Outline each Plasmodium vivax-infected red blood cell.
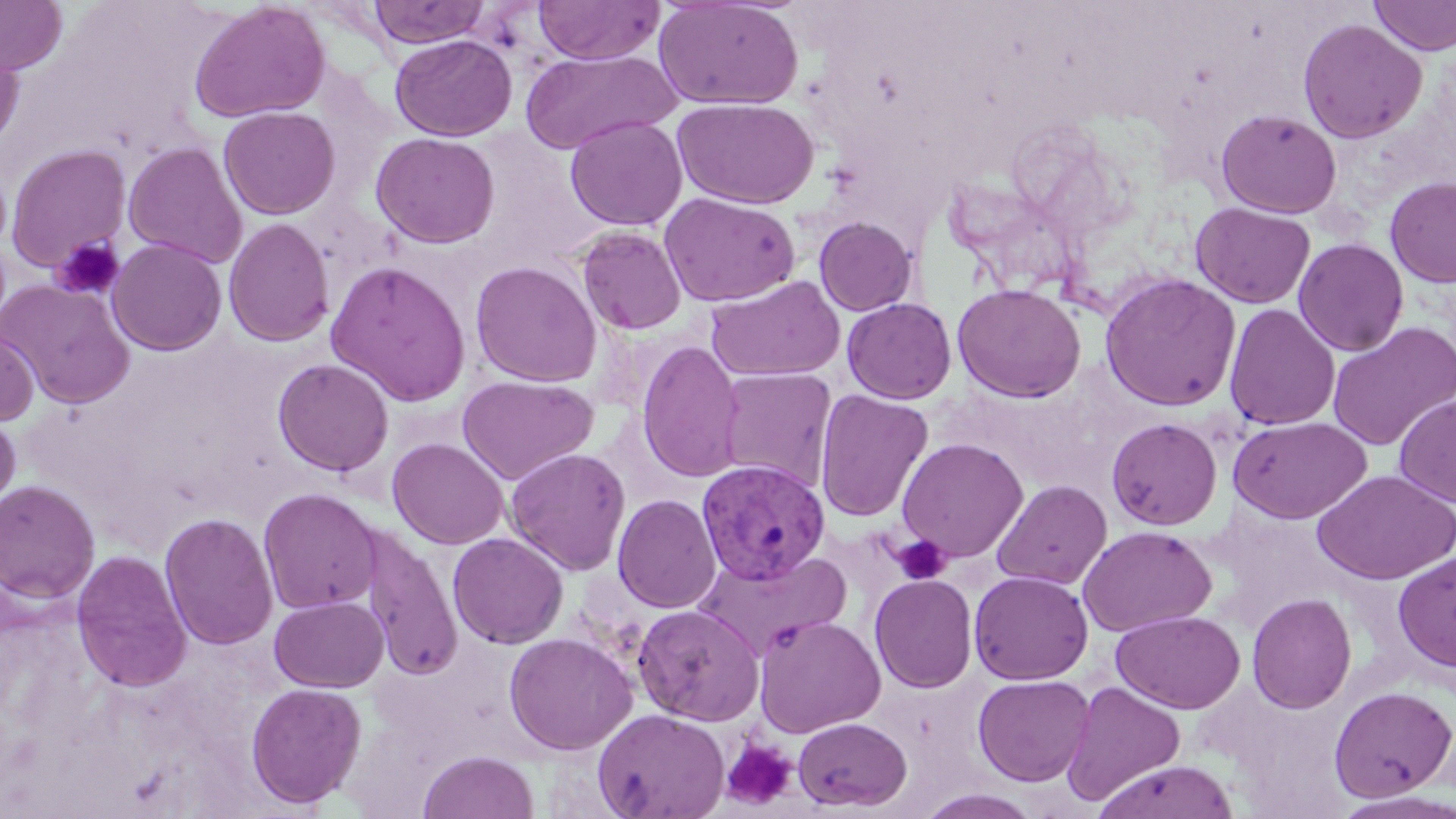
Approximate bounding boxes as [x1, y1, x2, y2] in pixels.
Plasmodium vivax-infected red blood cells: [696, 459, 831, 586].

slide-level diagnosis = Plasmodium vivax
image size = 1456×819 pixels
stain = May-Grünwald-Giemsa
magnification = 1000x
uninfected red blood cell locations = approximate bounding boxes as [x1, y1, x2, y2] in pixels: [0, 0, 69, 75], [368, 0, 490, 47], [533, 0, 664, 65], [1369, 0, 1456, 56], [188, 1, 332, 123], [653, 1, 804, 110], [1297, 17, 1427, 143], [390, 34, 517, 141], [0, 36, 25, 153], [520, 48, 678, 155], [672, 97, 819, 209], [218, 106, 340, 220], [1215, 108, 1342, 218], [565, 115, 687, 231], [370, 131, 501, 248], [123, 142, 248, 269], [5, 143, 131, 273], [1385, 176, 1456, 288], [659, 192, 801, 307], [1190, 202, 1316, 309], [813, 216, 918, 316], [223, 217, 335, 347], [576, 226, 687, 336], [106, 238, 228, 356], [1293, 238, 1409, 356], [324, 260, 472, 406], [470, 260, 602, 387], [1099, 273, 1241, 412], [705, 275, 846, 382], [1, 280, 136, 408], [952, 283, 1087, 402], [842, 297, 957, 403], [1224, 303, 1340, 430], [1327, 322, 1455, 451], [0, 326, 39, 427], [636, 339, 745, 483], [272, 358, 394, 476], [717, 368, 837, 490], [456, 374, 598, 486], [814, 388, 934, 523], [1394, 394, 1456, 507], [0, 410, 21, 520], [1229, 416, 1372, 524], [1106, 417, 1223, 530], [387, 437, 509, 549], [896, 438, 1028, 562], [504, 447, 631, 576], [1311, 468, 1456, 584], [991, 479, 1112, 589], [0, 480, 101, 603], [258, 488, 382, 614], [612, 494, 721, 613], [159, 511, 279, 651], [1077, 525, 1217, 636], [359, 527, 462, 681], [448, 532, 569, 649], [71, 549, 193, 693], [696, 550, 852, 661], [1393, 552, 1456, 673], [969, 570, 1094, 685], [869, 573, 978, 693], [1247, 592, 1357, 714], [269, 595, 388, 692], [632, 603, 764, 725], [1111, 610, 1246, 713], [754, 614, 886, 737], [504, 632, 638, 755], [972, 674, 1094, 786], [1061, 681, 1186, 806], [245, 682, 366, 808], [1328, 685, 1456, 801], [592, 708, 730, 819], [793, 716, 912, 812], [418, 750, 539, 819], [1092, 759, 1241, 819], [914, 789, 1045, 819]
platelet locations = approximate bounding boxes as [x1, y1, x2, y2] in pixels: [51, 236, 125, 301], [892, 535, 952, 584], [720, 738, 797, 811]
field of view = one of a larger specimen
modality = optical microscopy
preparation = thin blood film